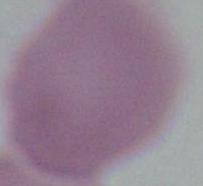

modality = micrograph
identification = red blood cell
magnification = 1000x